Give the extent of all Babesia divergens-infected red blood cells.
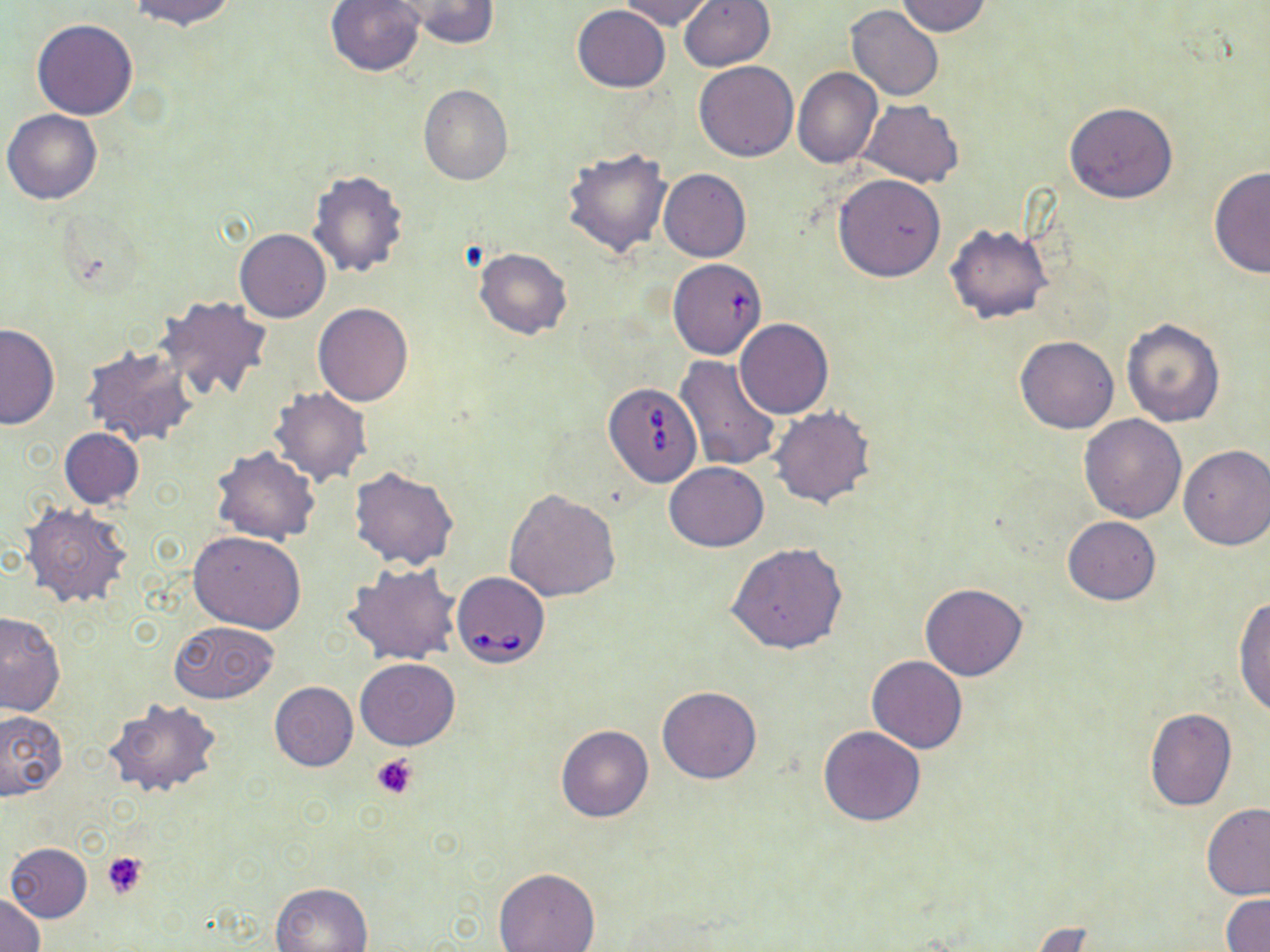
Approximate bounding boxes as named x1/y1/x2/y2 corners in pixels.
Babesia divergens-infected red blood cells: (x1=606, y1=380, x2=704, y2=487), (x1=452, y1=572, x2=549, y2=668).

Summary:
  - Platelet locations: (x1=371, y1=753, x2=419, y2=798), (x1=101, y1=851, x2=148, y2=900)
  - Uninfected red blood cell locations: (x1=128, y1=0, x2=238, y2=30), (x1=399, y1=0, x2=498, y2=48), (x1=677, y1=0, x2=775, y2=72), (x1=895, y1=0, x2=992, y2=36), (x1=324, y1=1, x2=427, y2=76), (x1=619, y1=1, x2=713, y2=28), (x1=572, y1=5, x2=670, y2=92), (x1=846, y1=5, x2=944, y2=100), (x1=31, y1=19, x2=138, y2=119), (x1=694, y1=60, x2=798, y2=162), (x1=793, y1=67, x2=882, y2=168), (x1=418, y1=83, x2=513, y2=185), (x1=861, y1=100, x2=964, y2=187), (x1=1064, y1=103, x2=1176, y2=204), (x1=2, y1=109, x2=102, y2=204), (x1=562, y1=145, x2=673, y2=257), (x1=1207, y1=166, x2=1270, y2=278), (x1=307, y1=169, x2=409, y2=279), (x1=659, y1=169, x2=751, y2=262), (x1=833, y1=173, x2=947, y2=282), (x1=944, y1=224, x2=1052, y2=324), (x1=235, y1=228, x2=330, y2=322), (x1=473, y1=246, x2=573, y2=340), (x1=667, y1=263, x2=769, y2=360), (x1=157, y1=295, x2=274, y2=403), (x1=312, y1=303, x2=413, y2=406), (x1=1120, y1=317, x2=1225, y2=427), (x1=735, y1=319, x2=833, y2=418), (x1=0, y1=324, x2=59, y2=430), (x1=1015, y1=334, x2=1118, y2=434), (x1=81, y1=344, x2=197, y2=447), (x1=675, y1=356, x2=784, y2=472), (x1=269, y1=386, x2=372, y2=487), (x1=769, y1=405, x2=875, y2=509), (x1=1079, y1=414, x2=1188, y2=523), (x1=58, y1=428, x2=144, y2=508), (x1=1178, y1=445, x2=1270, y2=550), (x1=211, y1=447, x2=321, y2=545), (x1=664, y1=461, x2=768, y2=552), (x1=349, y1=466, x2=460, y2=570), (x1=504, y1=489, x2=621, y2=602), (x1=21, y1=502, x2=133, y2=610), (x1=1063, y1=516, x2=1161, y2=605), (x1=188, y1=530, x2=306, y2=634), (x1=727, y1=543, x2=848, y2=654), (x1=345, y1=564, x2=460, y2=665), (x1=920, y1=582, x2=1026, y2=680), (x1=1234, y1=597, x2=1270, y2=719), (x1=0, y1=613, x2=65, y2=716), (x1=168, y1=620, x2=280, y2=704), (x1=867, y1=656, x2=966, y2=754), (x1=355, y1=658, x2=460, y2=750), (x1=268, y1=673, x2=455, y2=761), (x1=269, y1=682, x2=358, y2=771), (x1=658, y1=685, x2=762, y2=783), (x1=103, y1=697, x2=221, y2=798), (x1=1144, y1=709, x2=1237, y2=811), (x1=0, y1=710, x2=67, y2=801), (x1=556, y1=725, x2=653, y2=822), (x1=819, y1=725, x2=925, y2=827), (x1=1201, y1=803, x2=1270, y2=899), (x1=4, y1=843, x2=94, y2=922), (x1=494, y1=867, x2=600, y2=952), (x1=271, y1=881, x2=373, y2=951), (x1=0, y1=891, x2=45, y2=952), (x1=1220, y1=893, x2=1269, y2=952), (x1=1025, y1=922, x2=1100, y2=951)
  - Slide-level diagnosis: Babesia divergens
  - Modality: optical microscopy
  - Magnification: 1000x
  - Preparation: thin blood smear
  - Stain: May-Grünwald-Giemsa
  - Field of view: single
  - Image size: 1270×952 pixels